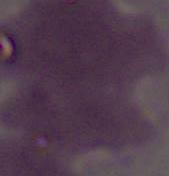
Captured at 1000x magnification. Photomicrograph. An erythrocyte is shown.